State the blood parasite species.
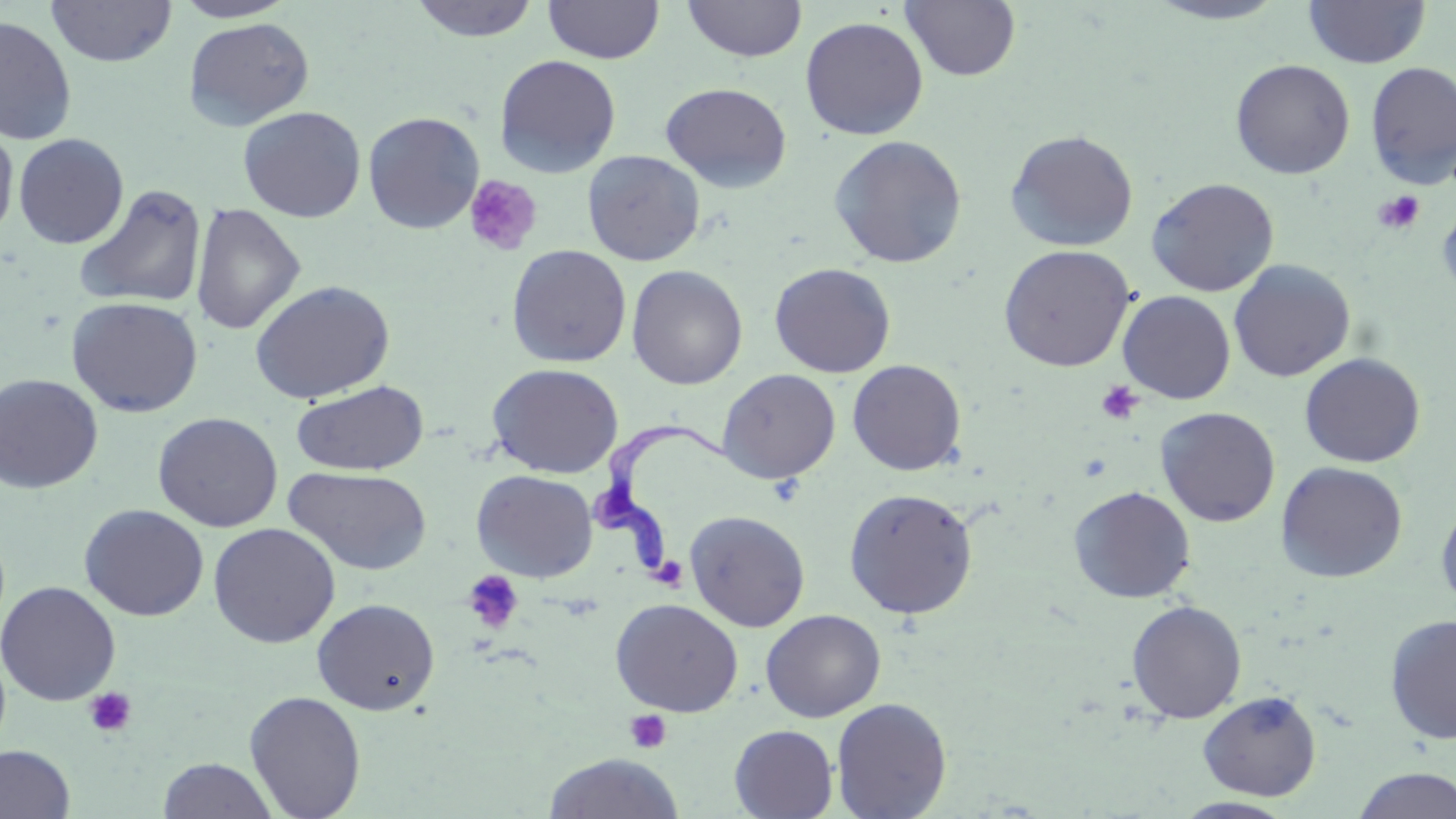
Trypanosoma brucei.

stain = May-Grünwald-Giemsa
field of view = single
image size = 1456×819 pixels
uninfected red blood cell locations = approximate bounding boxes as [x1, y1, x2, y2] in pixels: [47, 0, 177, 67], [170, 0, 300, 22], [409, 0, 541, 42], [544, 0, 664, 64], [682, 0, 807, 62], [899, 0, 1021, 82], [1145, 0, 1292, 25], [1303, 0, 1430, 69], [0, 14, 77, 146], [800, 16, 928, 141], [183, 17, 315, 131], [494, 54, 621, 178], [1230, 59, 1356, 179], [1365, 61, 1456, 188], [660, 82, 792, 193], [238, 106, 366, 223], [362, 111, 484, 234], [0, 122, 19, 243], [1005, 129, 1139, 252], [13, 133, 129, 249], [829, 134, 968, 269], [582, 150, 705, 266], [1146, 177, 1280, 297], [74, 184, 208, 309], [190, 202, 306, 335], [1437, 202, 1456, 306], [506, 244, 632, 368], [997, 244, 1136, 372], [1228, 259, 1356, 382], [769, 262, 896, 377], [626, 264, 748, 390], [250, 279, 395, 404], [1118, 290, 1236, 404], [66, 296, 203, 417], [1299, 352, 1426, 468], [847, 359, 967, 475], [487, 363, 623, 478], [717, 368, 841, 484], [0, 373, 104, 494], [291, 381, 429, 476], [1155, 406, 1281, 527], [152, 411, 284, 532], [1276, 461, 1409, 583], [283, 466, 433, 576], [471, 469, 598, 582], [1068, 485, 1196, 603], [843, 487, 978, 619], [1435, 496, 1456, 612], [79, 504, 209, 621], [685, 510, 811, 632], [207, 522, 341, 648], [0, 581, 121, 706], [312, 597, 440, 715], [610, 598, 743, 717], [1126, 600, 1247, 723], [761, 609, 886, 722], [1384, 614, 1456, 745], [1197, 689, 1322, 801], [244, 690, 366, 819], [831, 697, 952, 819], [729, 724, 838, 818], [0, 744, 76, 819], [544, 753, 684, 818], [157, 757, 279, 819], [1351, 767, 1456, 818], [1173, 797, 1298, 818]
preparation = thin blood film
Trypanosoma brucei locations = approximate bounding boxes as [x1, y1, x2, y2] in pixels: [593, 421, 732, 573]
modality = light microscopy
platelet locations = approximate bounding boxes as [x1, y1, x2, y2] in pixels: [463, 175, 543, 257], [1373, 190, 1426, 235], [1096, 381, 1142, 424], [656, 556, 689, 590], [462, 570, 524, 634], [83, 687, 137, 737], [624, 710, 672, 754]
magnification = 1000x